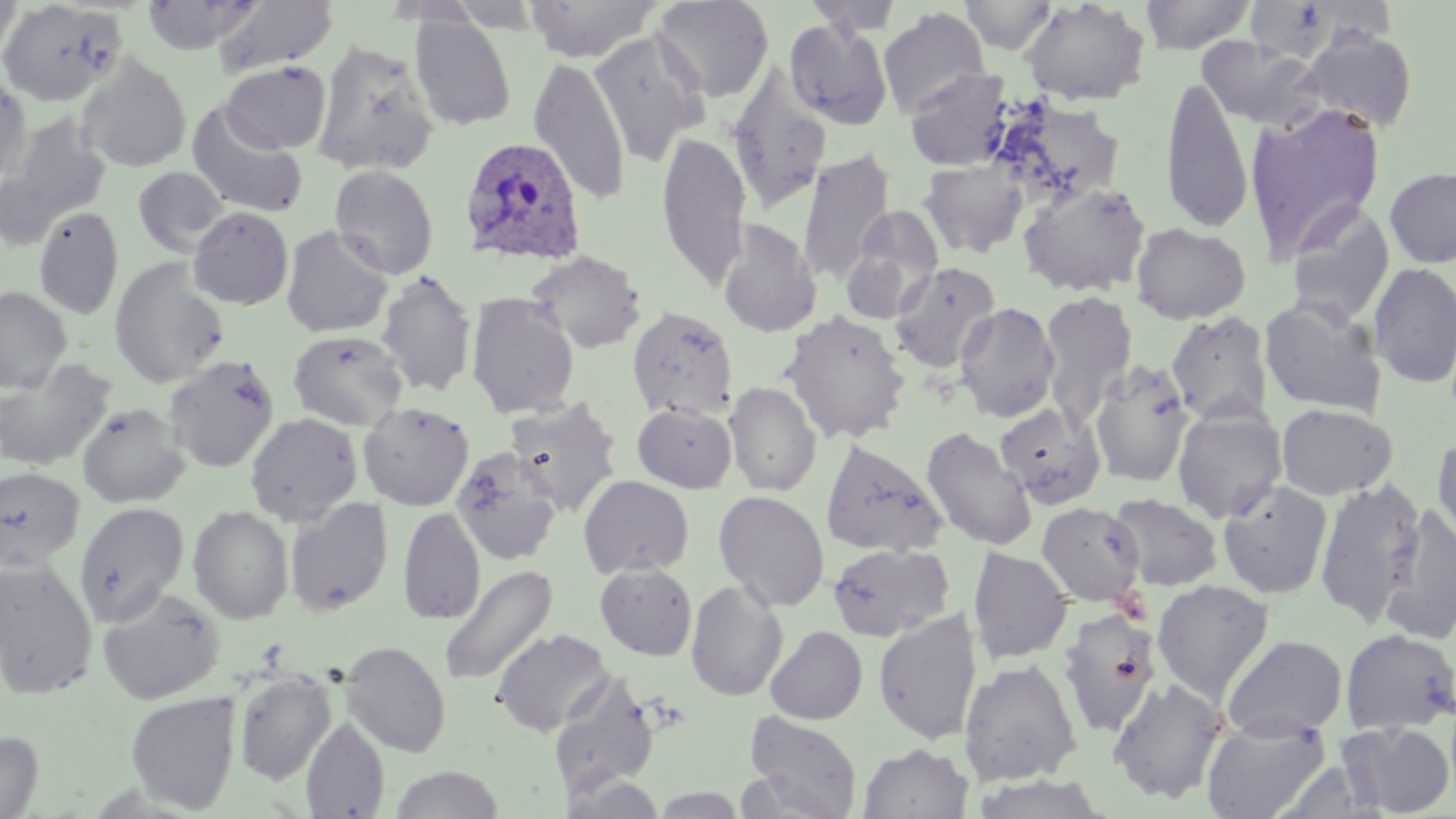
Approximate bounding boxes as (x1, y1, x2, y2) in pixels. Plasmodium ovale-infected red blood cell locations: (459, 138, 587, 267). Uninfected red blood cell locations: (0, 0, 23, 67), (213, 0, 338, 78), (524, 0, 662, 62), (651, 0, 774, 103), (802, 0, 905, 36), (960, 0, 1058, 55), (1139, 0, 1257, 54), (1019, 1, 1151, 106), (0, 2, 126, 107), (877, 7, 990, 119), (408, 14, 517, 131), (784, 20, 893, 129), (588, 30, 710, 165), (1301, 30, 1418, 133), (1196, 36, 1324, 132), (312, 40, 439, 176), (75, 55, 191, 172), (529, 57, 631, 206), (220, 61, 330, 154), (727, 68, 832, 213), (904, 68, 1015, 172), (0, 70, 31, 186), (1161, 76, 1254, 235), (999, 101, 1127, 204), (1244, 102, 1387, 260), (186, 104, 309, 220), (2, 113, 112, 242), (656, 131, 752, 291), (797, 148, 895, 285), (918, 159, 1030, 259), (329, 165, 438, 279), (1384, 165, 1456, 269), (133, 166, 229, 258), (1017, 181, 1151, 297), (1285, 201, 1395, 326), (33, 206, 124, 320), (845, 206, 945, 319), (187, 207, 294, 310), (717, 221, 822, 338), (1130, 223, 1251, 325), (280, 226, 393, 338), (526, 250, 647, 355), (108, 259, 229, 389), (888, 261, 1001, 373), (1368, 262, 1456, 388), (375, 270, 478, 397), (0, 286, 71, 392), (1038, 291, 1138, 421), (466, 293, 580, 419), (1259, 296, 1387, 417), (954, 301, 1061, 423), (627, 305, 738, 421), (780, 311, 911, 444), (1166, 311, 1274, 426), (288, 329, 408, 431), (164, 354, 280, 473), (0, 358, 115, 472), (1090, 359, 1194, 488), (724, 382, 822, 496), (505, 398, 623, 517), (358, 401, 475, 511), (76, 403, 190, 509), (632, 403, 737, 493), (994, 403, 1106, 508), (1276, 403, 1398, 499), (1172, 407, 1288, 523), (245, 413, 363, 526), (254, 416, 386, 607), (921, 425, 1038, 552), (1432, 430, 1456, 549), (820, 439, 947, 558), (450, 446, 562, 564), (0, 467, 85, 570), (578, 475, 694, 579), (1314, 479, 1427, 627), (1217, 480, 1333, 599), (713, 490, 830, 612), (1107, 493, 1223, 591), (285, 497, 394, 617), (74, 502, 189, 622), (1036, 502, 1145, 605), (188, 505, 294, 624), (1380, 506, 1456, 646), (398, 507, 485, 625), (826, 543, 954, 642), (967, 546, 1073, 665), (0, 559, 98, 699), (439, 563, 558, 687), (595, 564, 697, 660), (1152, 579, 1275, 702), (686, 580, 788, 702), (96, 588, 225, 704), (1057, 607, 1162, 737), (874, 609, 983, 746), (765, 626, 868, 725), (492, 628, 613, 736), (1339, 628, 1456, 735), (1221, 634, 1348, 740), (340, 641, 451, 758), (958, 659, 1082, 786), (234, 670, 336, 786), (549, 672, 661, 798), (1107, 678, 1229, 804), (125, 692, 239, 814), (743, 712, 863, 819), (1201, 716, 1330, 819), (300, 717, 390, 818), (1337, 721, 1455, 816), (0, 731, 43, 818), (858, 743, 972, 819), (389, 765, 505, 818), (969, 773, 1114, 818), (563, 776, 667, 818), (649, 786, 749, 817). Slide-level diagnosis: Plasmodium ovale. Image is 1456×819 pixels. Optical microscopy. Thin blood film. May-Grünwald-Giemsa stain. One field of a larger specimen. Captured at 1000x magnification.